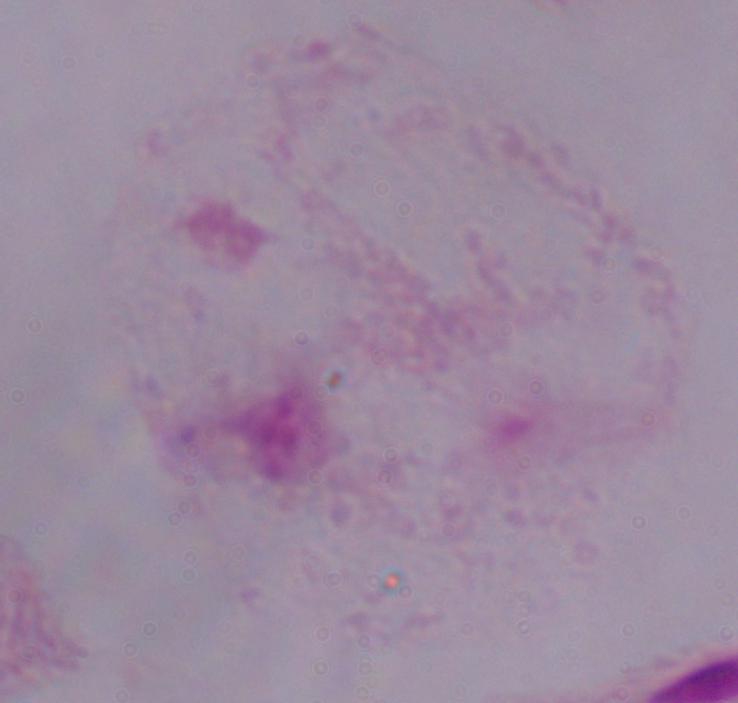
Summary:
  - Magnification: 1000x
  - Identification: trichomonad
  - Modality: photomicrograph